State which parasite is depicted.
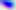

This is Toxoplasma gondii.

400x magnification. Micrograph.